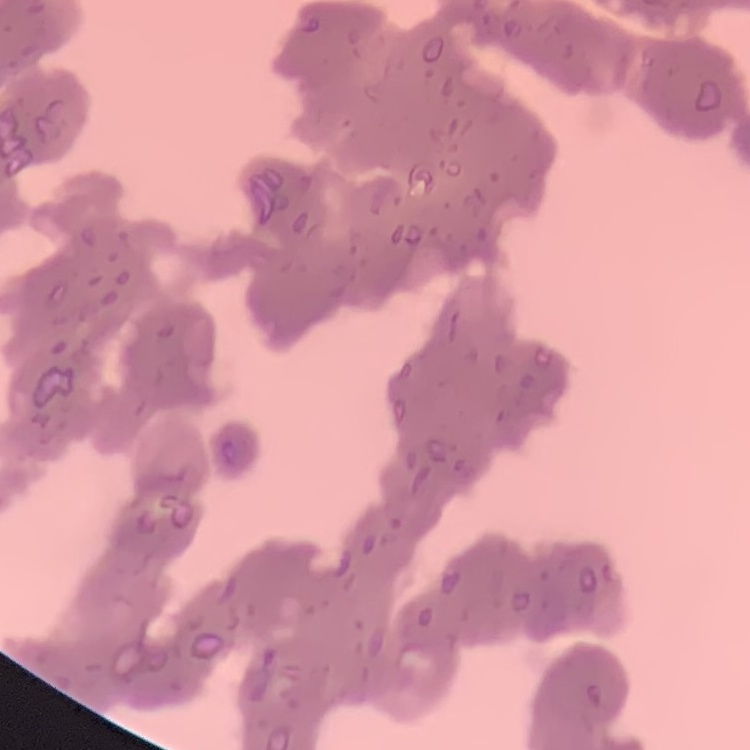
red blood cell morphology = rouleaux formation
stain = Field's or Giemsa
image type = one tile cut from a larger photomicrograph
preparation = thin peripheral smear